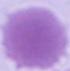

Summary:
  - Modality: micrograph
  - Magnification: 1000x
  - Identification: red blood cell